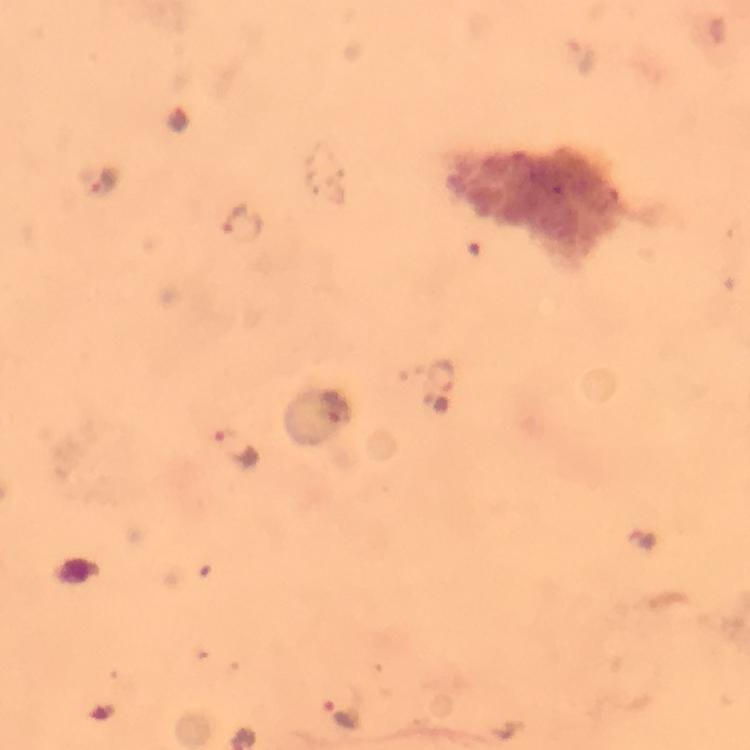
preparation = thick blood film
cropped from = one field of view
Plasmodium parasite locations = approximate centers as [x, y] in pixels: [582, 57], [180, 119], [105, 181], [243, 223], [442, 374], [335, 406], [240, 448], [341, 712]
context = from a malaria diagnostic workup
magnification = 100x
image size = 750×750 pixels
capture = smartphone camera through the microscope
stain = Giemsa
immersion oil = used